Locate and identify every blood parasite.
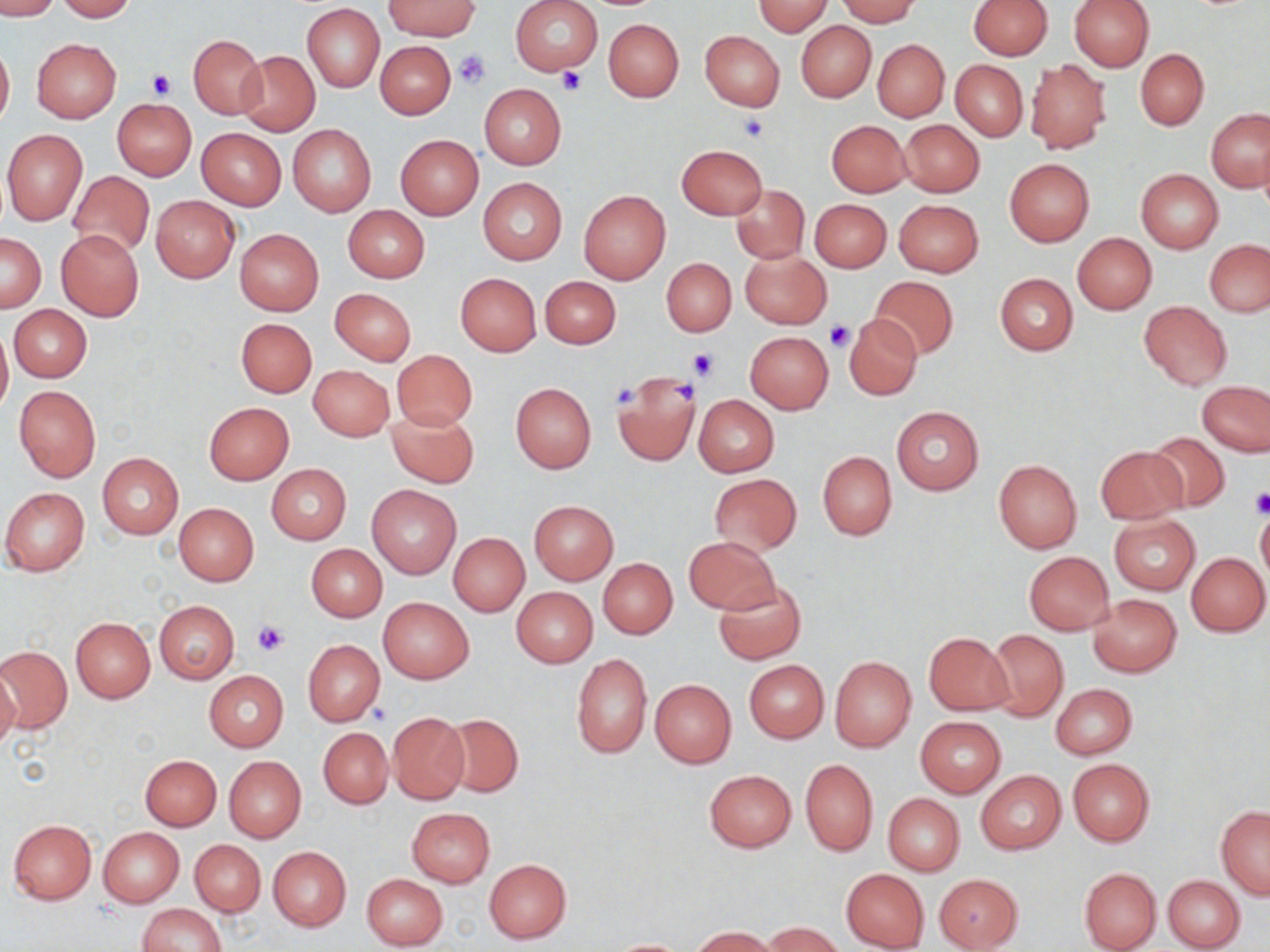

No blood parasites seen.

Summary:
  - Coordinate format: approximate bounding boxes as (x1, y1, x2, y2) in pixels
  - Platelet locations: (453, 48, 492, 89), (555, 65, 589, 96), (146, 69, 176, 98), (737, 112, 770, 143), (827, 321, 855, 351), (688, 348, 717, 382), (670, 380, 699, 405), (610, 382, 639, 410), (1249, 491, 1270, 518), (252, 619, 291, 657)
  - Uninfected red blood cell locations: (0, 0, 59, 19), (56, 0, 138, 22), (510, 0, 603, 76), (835, 0, 920, 25), (968, 0, 1052, 59), (1069, 0, 1154, 71), (384, 1, 481, 39), (755, 1, 830, 36), (303, 4, 384, 93), (604, 19, 683, 102), (796, 22, 875, 102), (699, 31, 785, 111), (189, 34, 266, 119), (32, 38, 121, 123), (873, 39, 949, 121), (0, 40, 14, 130), (375, 42, 455, 119), (1136, 48, 1208, 129), (236, 51, 319, 135), (951, 60, 1027, 142), (1025, 60, 1111, 154), (479, 84, 566, 168), (113, 99, 196, 180), (1207, 110, 1270, 193), (900, 119, 984, 197), (826, 120, 911, 197), (288, 124, 377, 216), (197, 128, 286, 210), (2, 130, 88, 225), (396, 135, 484, 219), (676, 144, 768, 219), (1004, 158, 1094, 246), (1136, 169, 1223, 254), (67, 170, 155, 259), (478, 178, 567, 264), (731, 185, 809, 264), (578, 189, 669, 284), (151, 196, 239, 282), (811, 199, 892, 273), (894, 199, 984, 277), (343, 205, 429, 283), (56, 229, 144, 321), (235, 229, 324, 315), (1, 233, 46, 312), (1073, 233, 1156, 314), (1204, 239, 1270, 317), (741, 250, 831, 328), (661, 259, 736, 336), (995, 272, 1078, 356), (455, 273, 542, 356), (869, 276, 960, 360), (540, 277, 619, 349), (330, 288, 416, 365), (1138, 302, 1232, 390), (9, 305, 91, 382), (844, 313, 922, 400), (235, 318, 317, 397), (0, 322, 12, 417), (745, 331, 834, 413), (391, 350, 478, 432), (309, 365, 394, 441), (611, 369, 703, 466), (1198, 380, 1270, 457), (510, 382, 597, 473), (14, 385, 101, 482), (692, 394, 780, 477), (204, 403, 294, 484), (891, 406, 984, 494), (386, 407, 478, 486), (1144, 431, 1231, 512), (1096, 445, 1187, 524), (818, 451, 896, 541), (98, 453, 183, 538), (994, 460, 1082, 553), (266, 463, 352, 545), (708, 473, 803, 556), (367, 485, 462, 579), (1, 487, 89, 577), (529, 500, 618, 586), (174, 503, 259, 585), (1256, 511, 1270, 591), (1109, 515, 1201, 595), (448, 532, 530, 616), (684, 536, 779, 614), (307, 545, 387, 622), (1023, 551, 1114, 634), (1186, 552, 1269, 636), (599, 558, 677, 638), (714, 579, 806, 664), (511, 587, 598, 667), (1087, 594, 1182, 677), (378, 597, 473, 683), (154, 600, 238, 683), (71, 618, 155, 703), (986, 629, 1068, 722), (923, 631, 1013, 715), (302, 639, 386, 725), (1, 642, 74, 734), (571, 653, 652, 760), (829, 656, 916, 751), (744, 660, 829, 742), (0, 667, 21, 755), (204, 671, 288, 752), (650, 679, 736, 768), (1051, 683, 1137, 759), (387, 712, 470, 804), (441, 714, 523, 798), (915, 717, 1005, 797), (318, 726, 393, 808), (140, 755, 221, 830), (224, 756, 306, 842), (1068, 759, 1155, 847), (800, 760, 877, 856), (704, 769, 796, 852), (975, 770, 1066, 855), (883, 793, 965, 877), (1217, 807, 1270, 899), (406, 808, 495, 887), (8, 819, 97, 903), (98, 827, 184, 907), (190, 839, 265, 916), (269, 846, 351, 930), (484, 859, 572, 943), (1079, 866, 1162, 951), (841, 868, 929, 950), (361, 872, 449, 950), (934, 873, 1023, 950), (1163, 875, 1245, 951), (137, 903, 227, 951), (761, 921, 843, 952), (690, 926, 784, 952), (608, 938, 692, 951)
  - Slide-level diagnosis: negative for blood parasites
  - Stain: May-Grünwald-Giemsa
  - Field of view: single
  - Preparation: thin blood smear
  - Magnification: 1000x
  - Modality: light microscopy
  - Image size: 1270×952 pixels